Identify the blood parasite species.
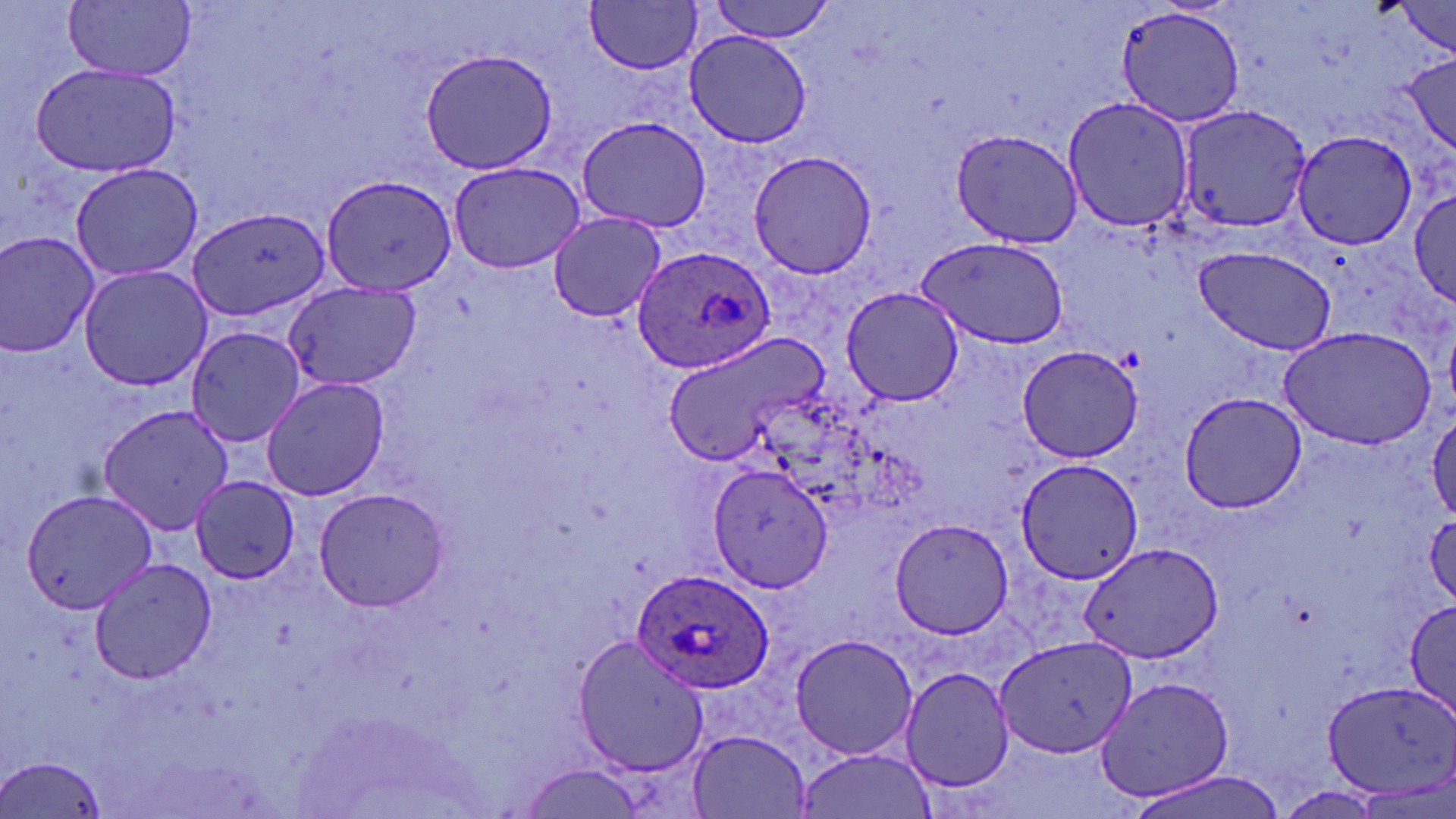
Plasmodium ovale.

preparation: thin blood film
plasmodium_ovale_infected_red_blood_cell_locations: 'approximate bounding boxes as (x1,y1)-(x2,y2) corner pairs in pixels: (633,247)-(776,373), (634,569)-(772,694)'
stain: May-Grünwald-Giemsa
modality: optical microscopy
magnification: 1000x
uninfected_red_blood_cell_locations: 'approximate bounding boxes as (x1,y1)-(x2,y2) corner pairs in pixels: (64,0)-(196,81), (708,0)-(835,43), (586,1)-(702,74), (1386,1)-(1453,58), (1116,6)-(1247,129), (684,30)-(812,149), (419,48)-(558,175), (1398,52)-(1456,155), (28,62)-(185,178), (1062,94)-(1194,234), (1176,104)-(1313,234), (577,116)-(709,234), (948,130)-(1083,246), (1289,131)-(1420,253), (747,150)-(879,279), (448,159)-(588,274), (67,160)-(203,282), (321,173)-(462,298), (1410,185)-(1454,308), (185,207)-(332,322), (547,212)-(665,321), (0,230)-(100,358), (917,235)-(1070,349), (1192,245)-(1336,354), (77,265)-(214,392), (283,282)-(419,391), (843,286)-(966,406), (1279,325)-(1440,447), (186,326)-(308,448), (664,332)-(830,468), (1015,345)-(1145,463), (260,376)-(389,500), (1178,391)-(1309,514), (97,401)-(233,536), (1428,411)-(1456,523), (1016,460)-(1140,583), (709,464)-(831,594), (188,475)-(300,584), (313,486)-(449,612), (18,487)-(158,615), (1425,511)-(1456,609), (890,518)-(1014,640), (1081,543)-(1221,663), (88,554)-(220,684), (1404,597)-(1456,722), (791,632)-(919,760), (571,635)-(708,776), (994,636)-(1136,759), (899,664)-(1017,793), (1094,675)-(1238,805), (1322,680)-(1456,799), (688,731)-(814,818), (798,750)-(932,819), (0,755)-(113,819), (516,765)-(650,818), (1126,767)-(1291,818)'
image_size: 1456×819 pixels
field_of_view: single